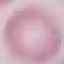
Result: no malaria parasites detected. Acquired by smartphone through the microscope eyepiece. Automatically extracted cell patch, resized to 64 × 64 pixels. Giemsa-stained preparation. Thin blood film.